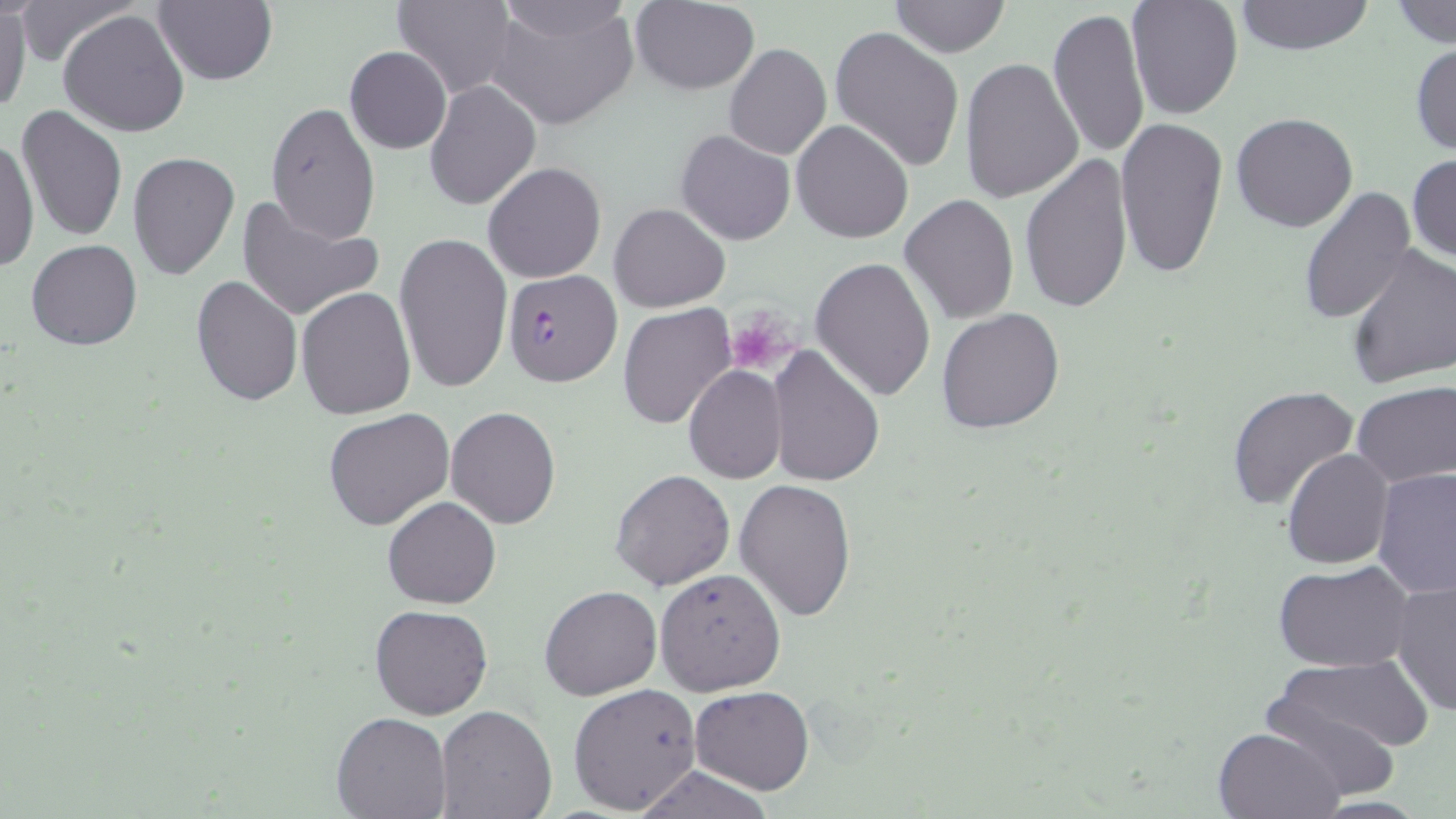
Summary:
  - Coordinate format: approximate bounding boxes as (x1,y1)-(x2,y2) corner pairs in pixels
  - Platelet locations: (731,320)-(790,379)
  - Uninfected red blood cell locations: (12,0)-(142,64), (153,0)-(275,87), (393,0)-(517,101), (494,0)-(633,39), (1125,0)-(1244,121), (1233,0)-(1375,54), (631,1)-(760,95), (888,1)-(1013,57), (1390,1)-(1455,48), (0,5)-(30,114), (484,5)-(641,129), (60,7)-(190,139), (1049,8)-(1150,162), (830,26)-(964,170), (1410,41)-(1456,158), (723,43)-(831,161), (345,46)-(450,154), (959,55)-(1083,202), (424,80)-(540,211), (265,103)-(381,246), (15,105)-(129,242), (1231,112)-(1359,234), (1115,116)-(1230,279), (792,118)-(913,244), (676,129)-(796,245), (1,136)-(38,272), (129,150)-(240,283), (1408,152)-(1456,265), (1021,157)-(1134,314), (482,162)-(606,284), (1298,185)-(1417,326), (901,193)-(1018,324), (235,196)-(382,323), (610,202)-(729,312), (392,230)-(513,393), (26,239)-(141,350), (1344,245)-(1456,391), (810,256)-(937,402), (190,275)-(303,408), (296,286)-(417,418), (619,304)-(737,432), (936,309)-(1064,434), (767,346)-(885,486), (682,365)-(786,483), (1351,382)-(1455,489), (1226,385)-(1360,509), (445,406)-(562,528), (322,408)-(455,531), (1281,449)-(1394,569), (1372,467)-(1455,598), (610,469)-(734,591), (734,478)-(857,622), (383,496)-(501,608), (1273,561)-(1416,672), (654,568)-(786,696), (1390,579)-(1455,717), (539,585)-(662,701), (369,603)-(493,719), (1265,655)-(1433,777), (567,683)-(704,814), (688,685)-(814,795), (434,707)-(559,819), (332,710)-(451,818), (1212,724)-(1347,819), (629,764)-(780,819)
  - Plasmodium falciparum-infected red blood cell locations: (502,270)-(621,388)
  - Slide-level diagnosis: Plasmodium falciparum
  - Field of view: one of a larger specimen
  - Magnification: 1000x
  - Image size: 1456×819 pixels
  - Modality: light microscopy
  - Preparation: thin blood film
  - Stain: May-Grünwald-Giemsa